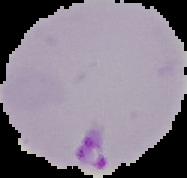
From a thin blood smear. Malaria status: parasitized. Segmented cell region on a black background. Image is 187×178 pixels.